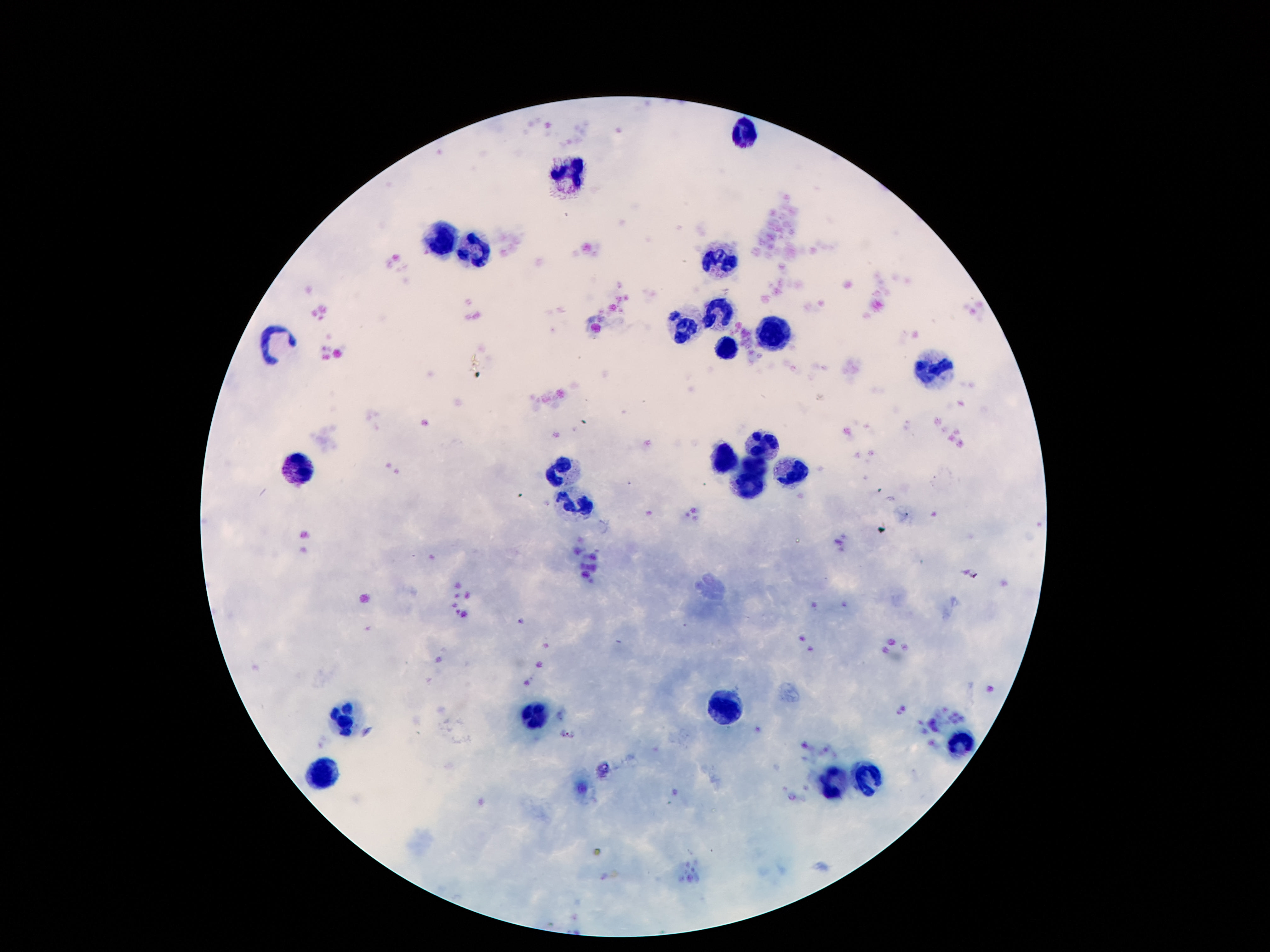
Approximate centers as [x, y] in pixels.
Summary:
  - Leukocyte locations: [748, 132], [569, 175], [439, 238], [474, 251], [717, 258], [717, 309], [682, 329], [770, 337], [279, 343], [726, 351], [934, 371], [768, 443], [726, 459], [753, 466], [560, 470], [297, 471], [792, 471], [750, 483], [578, 503], [724, 709], [536, 716], [348, 721], [963, 740], [324, 775], [872, 777], [837, 784]
  - Capture: smartphone camera through the microscope eyepiece
  - Field of view: single
  - Magnification: 100x
  - Preparation: thick blood film
  - Patient malaria status: negative
  - Image size: 1270×952 pixels
  - Stain: Giemsa